Assess this cell for malaria.
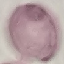

It is uninfected.

Summary:
  - Stain: Giemsa
  - Image type: automatically extracted cell patch, resized to 64 × 64 pixels
  - Preparation: thin smear
  - Capture: smartphone camera at the microscope eyepiece